Assess for malaria.
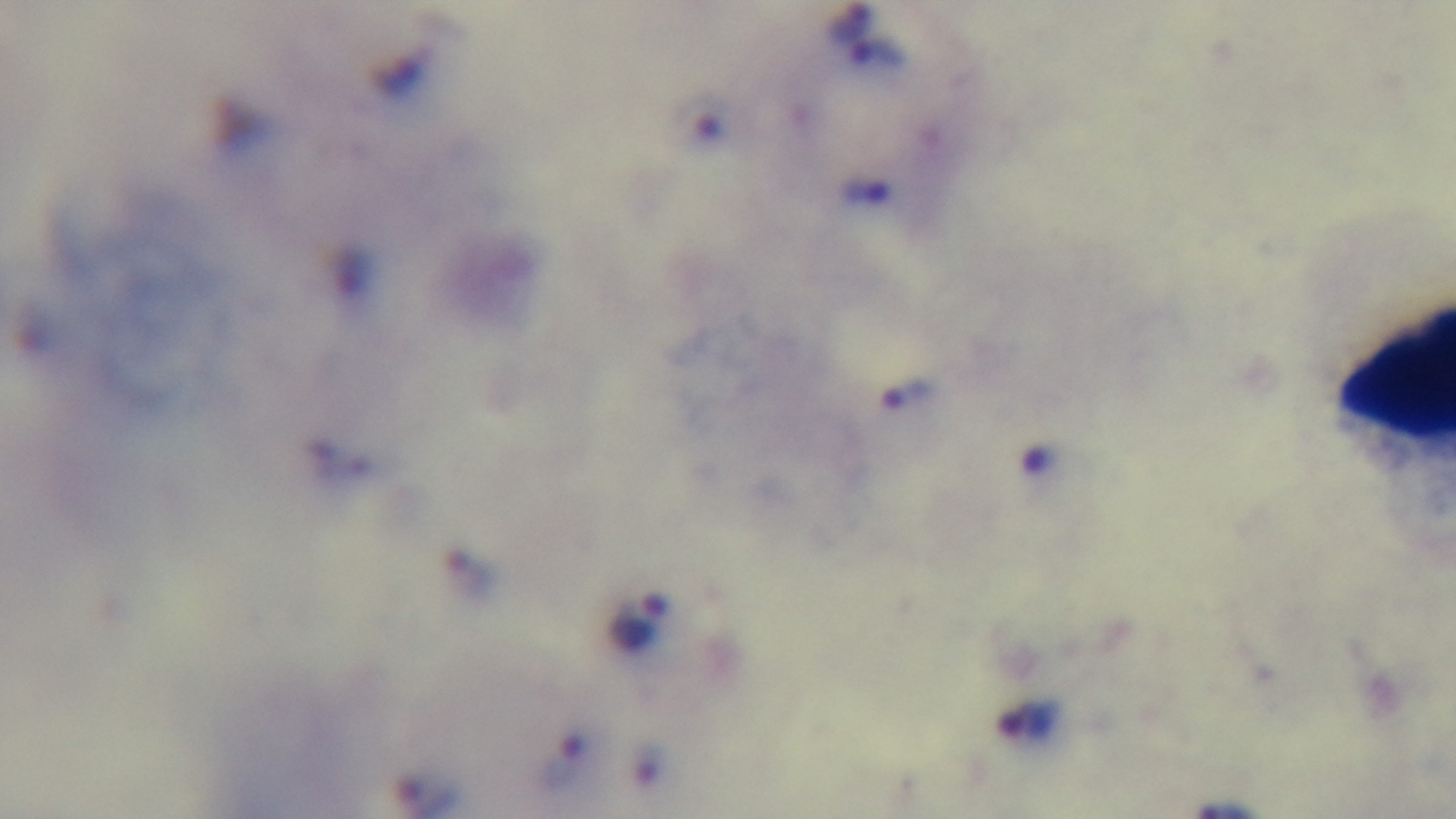

It is infected.

Mounted 4K digital camera. Light microscopy. Preparation: thick smear. 100x oil-immersion objective. Single field of view. Giemsa stain.